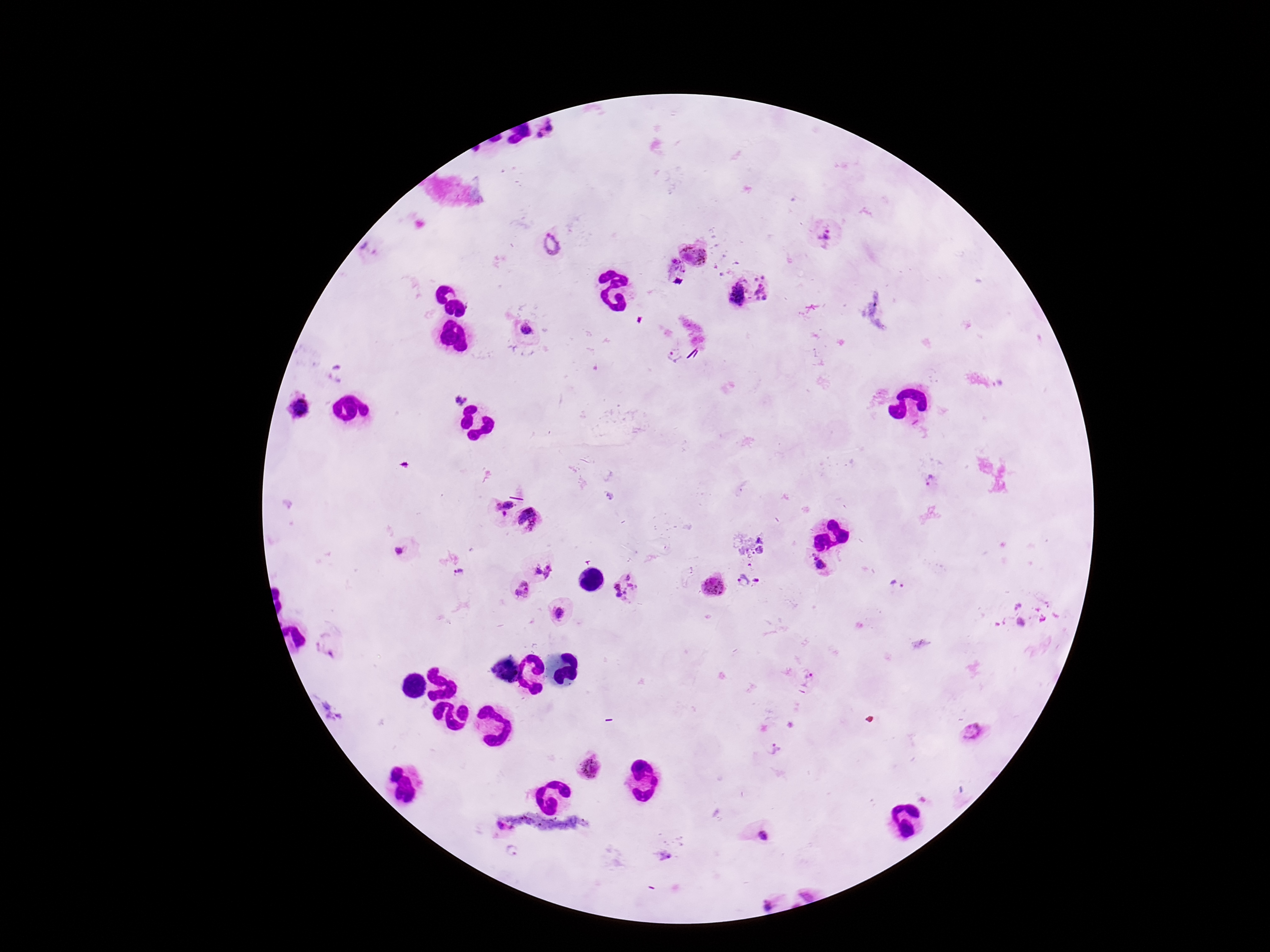
{
  "preparation": "thick blood smear",
  "stain": "Giemsa",
  "patient_malaria_status": "infected",
  "plasmodium_parasite_locations": "approximate object centers, in pixels from the top-left corner: (x=550, y=133), (x=824, y=235), (x=554, y=243), (x=697, y=251), (x=673, y=274), (x=768, y=285), (x=735, y=294), (x=527, y=331), (x=673, y=355), (x=458, y=399), (x=299, y=408), (x=499, y=504), (x=531, y=519), (x=399, y=550), (x=819, y=564), (x=544, y=570), (x=459, y=572), (x=743, y=581), (x=895, y=584), (x=713, y=586), (x=626, y=589), (x=522, y=590), (x=1016, y=604), (x=559, y=613), (x=1022, y=624), (x=810, y=677), (x=972, y=733), (x=772, y=751), (x=590, y=767), (x=502, y=831), (x=762, y=836), (x=513, y=851), (x=767, y=903)",
  "magnification": "100x",
  "field_of_view": "single",
  "capture": "smartphone camera through the microscope eyepiece",
  "image_size": "1270×952 pixels"
}